Locate and identify every blood parasite.
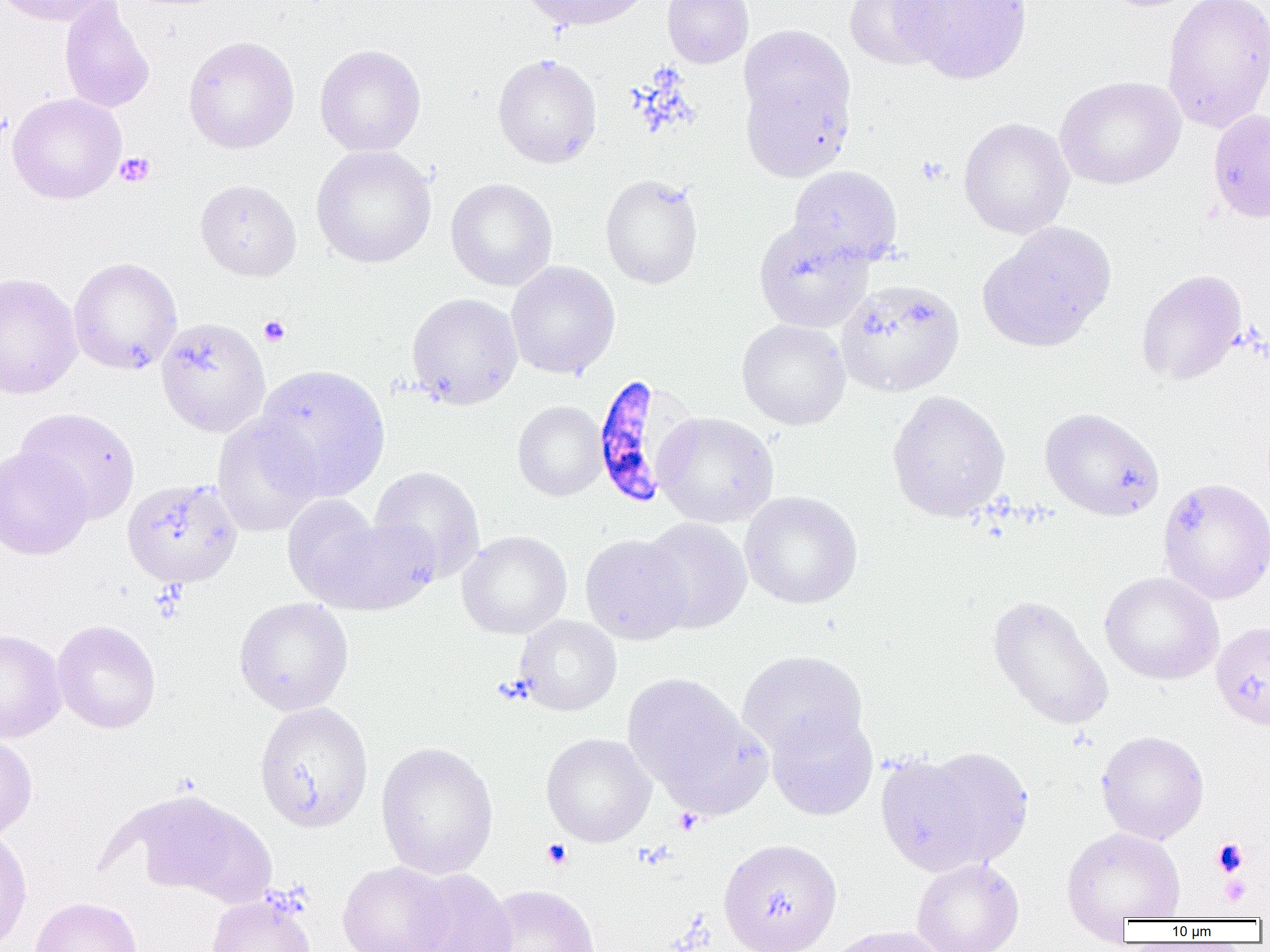

Approximate bounding boxes as [x1, y1, x2, y2] in pixels.
Plasmodium falciparum-infected red blood cells: [590, 375, 694, 509].
No Plasmodium ovale, Plasmodium malariae, Plasmodium vivax, Babesia divergens, or Trypanosoma brucei observed.

Summary:
  - Platelet locations: [115, 152, 155, 187], [915, 155, 948, 186], [258, 315, 291, 347], [674, 808, 703, 835], [1212, 838, 1249, 877], [542, 839, 572, 870], [1219, 876, 1250, 907]
  - Uninfected red blood cell locations: [0, 0, 111, 27], [58, 0, 155, 114], [519, 0, 654, 31], [662, 0, 754, 68], [844, 0, 951, 71], [893, 0, 1033, 85], [1093, 0, 1208, 12], [1161, 0, 1270, 134], [737, 25, 855, 135], [183, 35, 299, 154], [314, 44, 427, 157], [492, 54, 602, 168], [739, 67, 854, 182], [1055, 76, 1186, 190], [6, 92, 127, 204], [1207, 108, 1270, 224], [958, 117, 1074, 239], [311, 145, 437, 268], [787, 165, 903, 268], [600, 174, 703, 290], [446, 178, 557, 291], [195, 179, 302, 281], [753, 220, 874, 334], [977, 222, 1117, 352], [68, 257, 183, 375], [506, 261, 620, 379], [1136, 269, 1247, 385], [0, 272, 82, 399], [835, 279, 964, 397], [406, 292, 523, 410], [156, 317, 271, 437], [736, 319, 851, 430], [252, 363, 391, 501], [886, 389, 1011, 522], [512, 400, 607, 501], [15, 407, 140, 523], [1039, 407, 1165, 521], [653, 411, 779, 528], [212, 415, 322, 537], [0, 446, 93, 561], [370, 466, 485, 582], [121, 477, 243, 589], [1157, 477, 1270, 604], [740, 491, 863, 609], [282, 494, 386, 607], [325, 516, 441, 614], [640, 518, 752, 634], [456, 531, 572, 639], [580, 533, 691, 644], [1100, 571, 1224, 685], [987, 594, 1113, 730], [233, 597, 354, 716], [514, 615, 621, 716], [51, 619, 161, 734], [1211, 621, 1270, 729], [0, 627, 67, 743], [737, 649, 868, 759], [621, 672, 756, 802], [254, 701, 374, 833], [766, 711, 878, 820], [1096, 730, 1210, 844], [0, 733, 38, 842], [541, 733, 656, 847], [376, 741, 499, 879], [914, 745, 1034, 868], [874, 751, 991, 876], [0, 826, 33, 952], [1061, 826, 1187, 929], [718, 838, 842, 952], [911, 858, 1025, 952], [337, 860, 453, 952], [403, 869, 517, 952], [479, 884, 600, 952], [206, 894, 316, 952], [29, 896, 144, 952], [825, 925, 949, 952]
  - Slide-level diagnosis: Plasmodium falciparum
  - Modality: light microscopy
  - Field of view: one of a larger specimen
  - Magnification: 1000x
  - Image size: 1270×952 pixels
  - Preparation: thin blood smear